State which parasite is depicted.
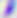

Toxoplasma gondii.

magnification = 400x
modality = micrograph